Assess this cell for malaria.
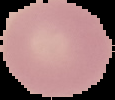

It is uninfected.

From a thin blood film. Image is 115×100 pixels. Segmented cell region on a black background.